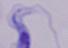
modality = micrograph
magnification = 1000x
identification = trypanosome